Report the malaria status.
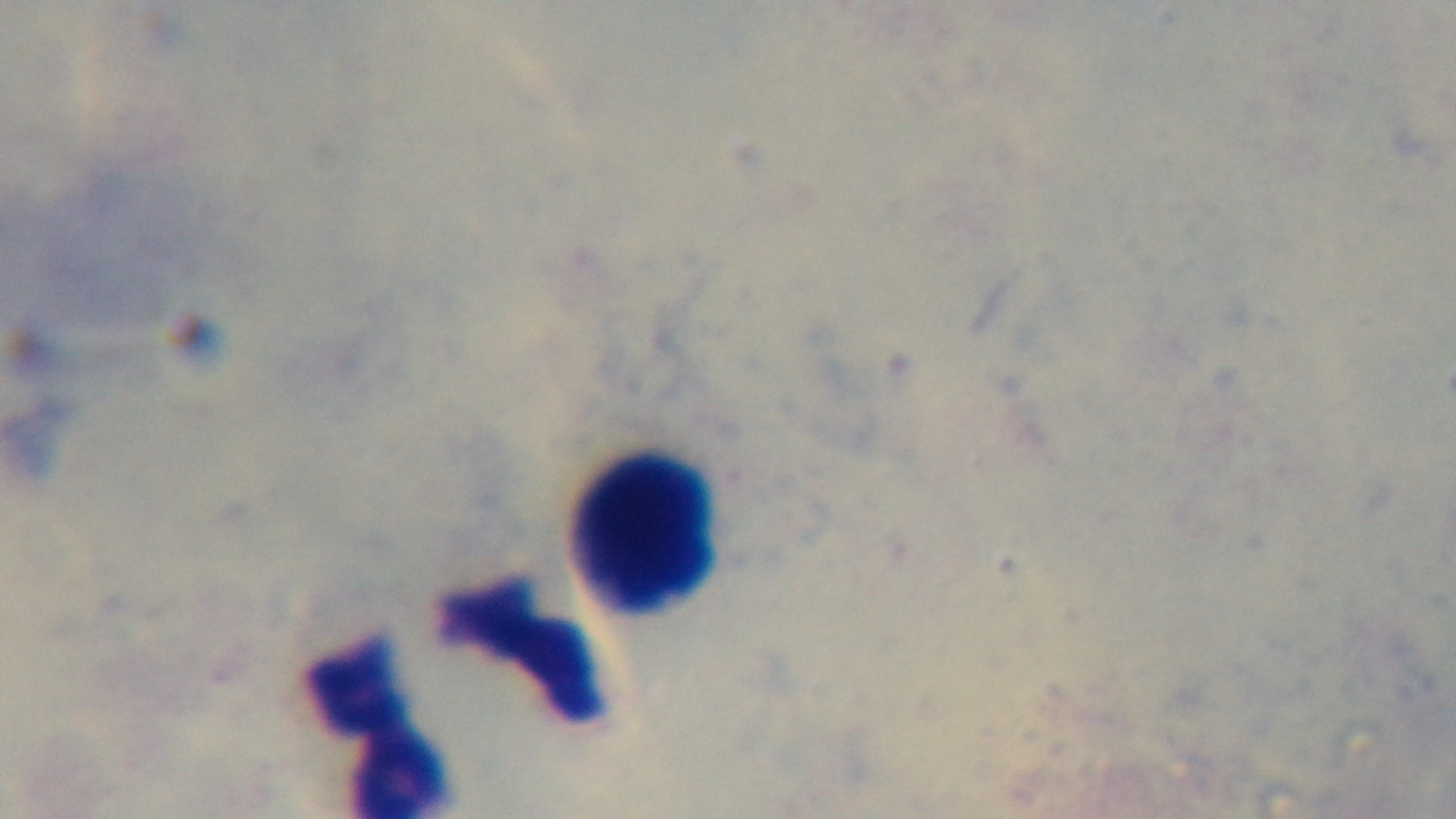
Uninfected.

Preparation: thick smear. Mounted 4K digital camera. Oil-immersion objective, 100x. Giemsa-stained. One field from the slide. Photomicrograph.